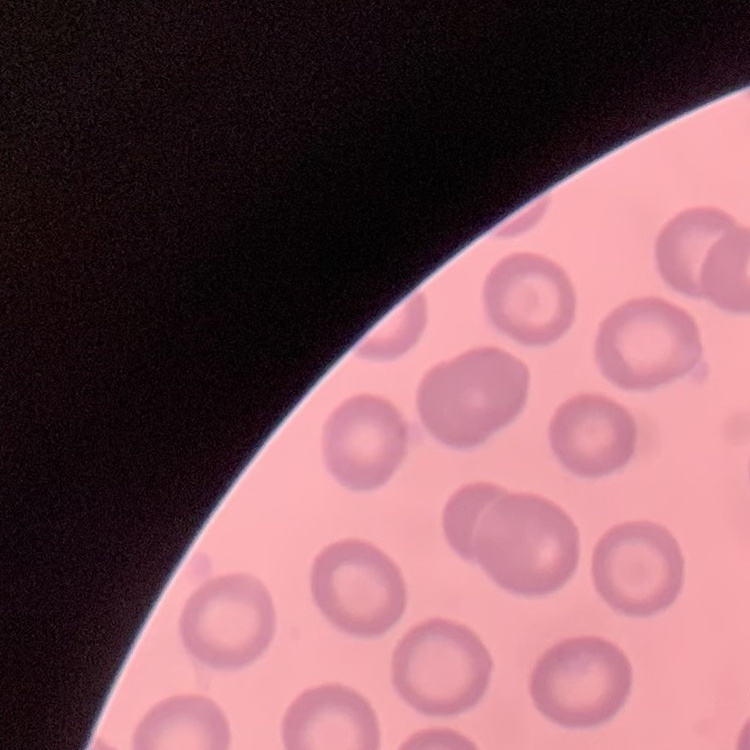
The red blood cells show no rouleaux formation. Field's or Giemsa stain. Thin peripheral smear. Square crop of a larger photomicrograph.